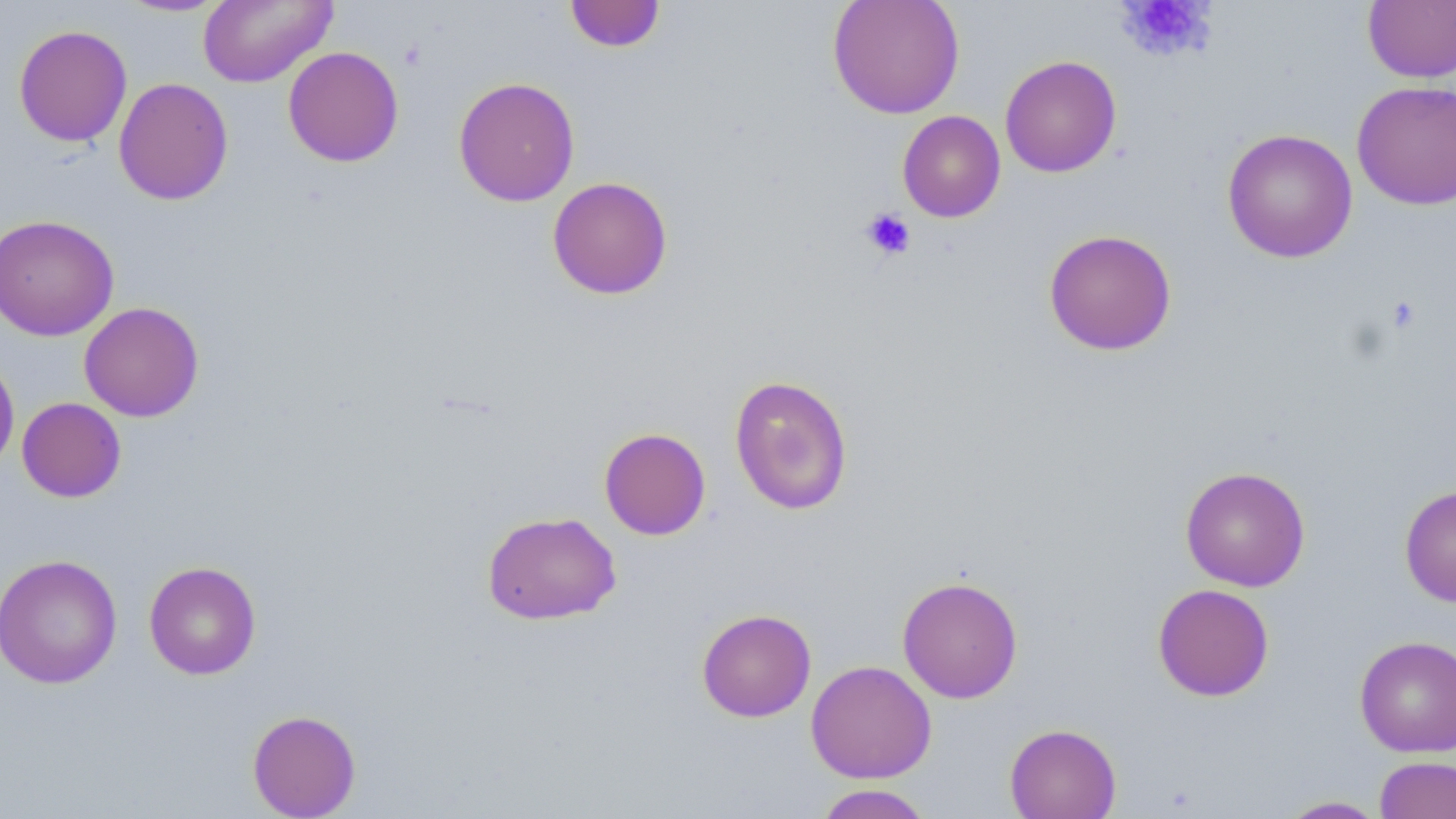
{
  "slide_level_diagnosis": "negative for blood parasites",
  "magnification": "1000x",
  "platelet_locations": "approximate bounding boxes as [x1, y1, x2, y2] in pixels: [1119, 0, 1215, 61], [860, 208, 916, 260], [1385, 295, 1422, 334]",
  "image_size": "1456×819 pixels",
  "preparation": "thin blood smear",
  "field_of_view": "single",
  "stain": "May-Grünwald-Giemsa",
  "uninfected_red_blood_cell_locations": "approximate bounding boxes as [x1, y1, x2, y2] in pixels: [114, 0, 231, 17], [197, 0, 338, 88], [827, 0, 965, 119], [564, 1, 666, 53], [1362, 1, 1456, 83], [13, 24, 132, 147], [283, 46, 404, 167], [999, 55, 1122, 178], [453, 76, 580, 206], [113, 77, 234, 206], [1351, 81, 1456, 210], [897, 110, 1006, 222], [1222, 128, 1358, 263], [547, 176, 673, 300], [0, 214, 119, 341], [1043, 228, 1177, 356], [79, 301, 204, 422], [0, 354, 20, 477], [729, 374, 853, 516], [16, 397, 126, 502], [598, 427, 711, 540], [1180, 466, 1311, 591], [1399, 484, 1456, 607], [482, 511, 621, 625], [0, 553, 122, 689], [144, 560, 262, 680], [897, 576, 1023, 703], [1153, 583, 1275, 701], [696, 608, 817, 722], [1354, 635, 1456, 757], [806, 660, 937, 783], [247, 709, 362, 818], [1005, 723, 1121, 819], [1374, 756, 1456, 818], [813, 784, 934, 818], [1276, 796, 1388, 818]",
  "modality": "light microscopy"
}